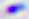

Toxoplasma gondii is seen. Micrograph. Captured at 400x magnification.